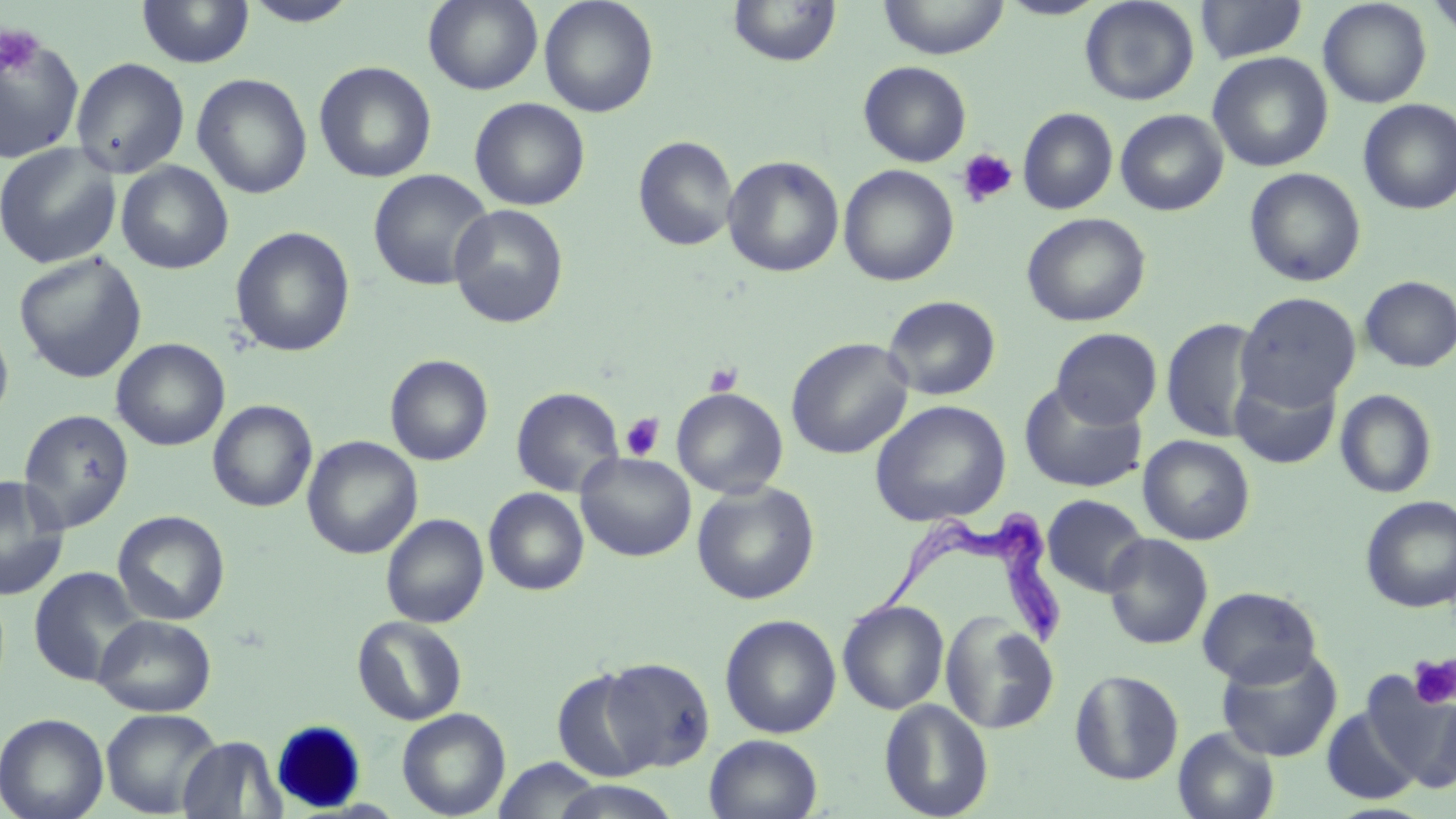 Approximate bounding boxes as (x1, y1, x2, y2) in pixels. Platelet locations: (0, 24, 44, 79), (956, 148, 1018, 208), (703, 362, 744, 397), (620, 412, 665, 461), (1408, 655, 1456, 709). Uninfected red blood cell locations: (423, 0, 543, 94), (539, 0, 659, 118), (878, 0, 1009, 59), (996, 0, 1109, 20), (1080, 0, 1199, 106), (1196, 0, 1308, 63), (1318, 0, 1432, 108), (136, 1, 254, 68), (240, 1, 360, 27), (728, 1, 842, 68), (0, 33, 85, 163), (1207, 52, 1333, 172), (70, 57, 190, 178), (314, 61, 437, 183), (858, 61, 972, 166), (192, 73, 312, 199), (469, 97, 590, 211), (1358, 99, 1456, 215), (1017, 107, 1118, 214), (1115, 109, 1228, 216), (633, 135, 738, 252), (0, 142, 122, 269), (722, 155, 844, 278), (116, 161, 234, 274), (838, 164, 959, 287), (1244, 167, 1366, 287), (368, 169, 493, 291), (448, 204, 569, 328), (1021, 212, 1151, 327), (229, 226, 356, 357), (14, 252, 147, 383), (1359, 276, 1456, 372), (1236, 292, 1361, 411), (882, 295, 1001, 401), (1161, 317, 1263, 443), (0, 318, 14, 430), (1051, 327, 1162, 429), (786, 337, 913, 459), (112, 338, 230, 451), (385, 354, 493, 466), (1230, 370, 1342, 469), (1018, 381, 1147, 493), (511, 387, 625, 497), (671, 387, 788, 499), (1335, 389, 1437, 499), (207, 399, 317, 512), (870, 399, 1011, 527), (17, 408, 134, 534), (1138, 435, 1255, 545), (302, 436, 422, 560), (575, 452, 696, 562), (0, 477, 70, 600), (692, 481, 820, 605), (484, 488, 589, 596), (1041, 494, 1150, 597), (1360, 496, 1456, 614), (113, 510, 230, 625), (381, 513, 489, 628), (1103, 533, 1213, 650), (29, 566, 146, 687), (1197, 586, 1321, 687), (837, 599, 950, 715), (940, 611, 1060, 735), (93, 614, 216, 716), (719, 614, 842, 739), (353, 616, 468, 725), (1216, 645, 1344, 762), (598, 657, 715, 772), (551, 667, 661, 782), (1069, 669, 1184, 785), (1361, 674, 1456, 791), (879, 699, 994, 818), (1321, 705, 1421, 805), (100, 708, 222, 817), (397, 708, 511, 818), (0, 713, 109, 819), (1173, 727, 1280, 819), (704, 734, 823, 819), (178, 736, 285, 818), (492, 757, 607, 819), (547, 780, 684, 819). Trypanosoma brucei locations: (850, 511, 1071, 654). Slide-level diagnosis: Trypanosoma brucei. Optical microscopy. Single field of view. Captured at 1000x magnification. Thin blood smear. Image is 1456×819 pixels. May-Grünwald-Giemsa-stained preparation.